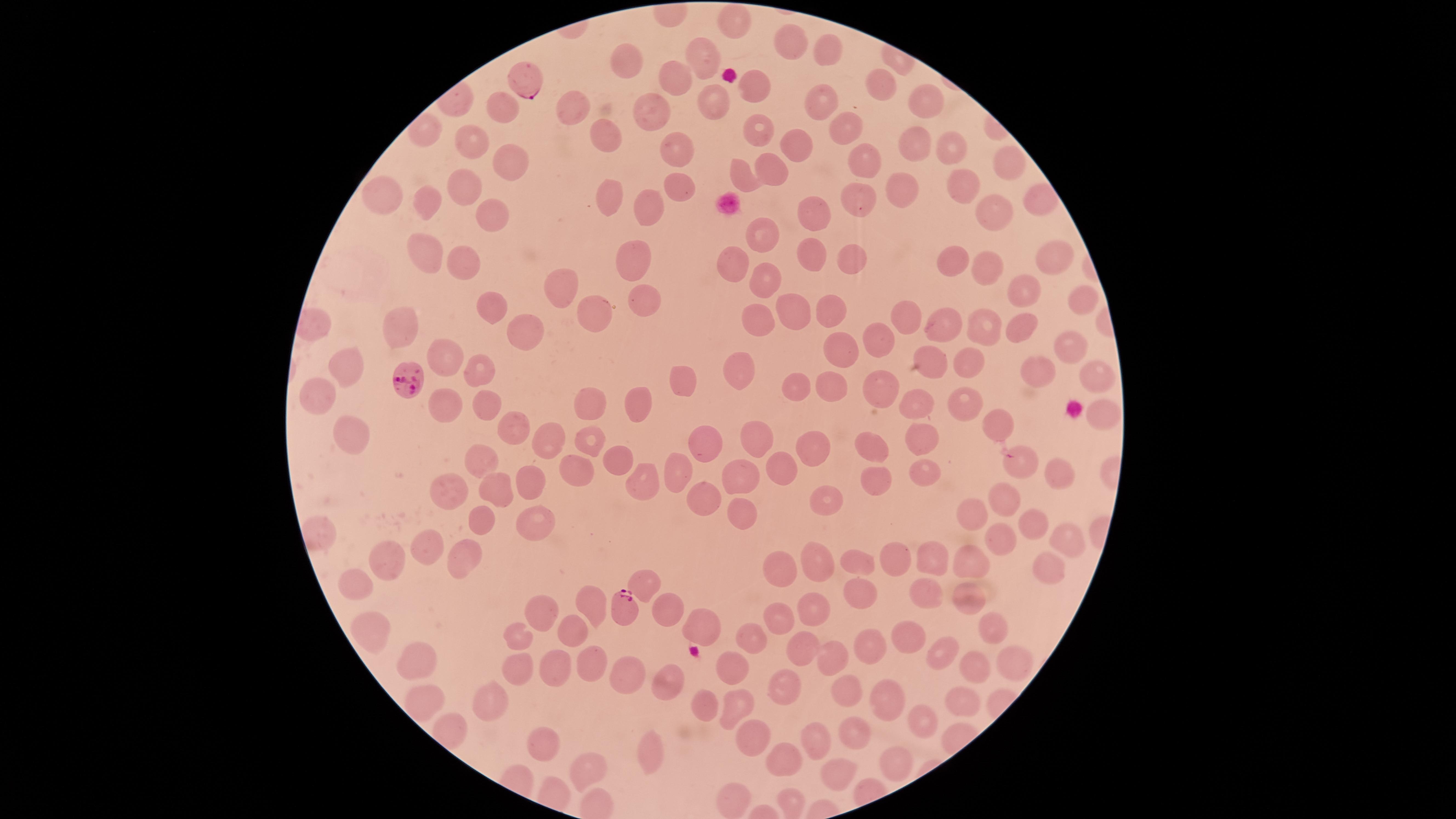

Approximate marker points as (x, y) in pixels.
Summary:
  - Parasitized red blood cells: (526, 73), (409, 384), (625, 611)
  - Uninfected red blood cells: (733, 25), (792, 40), (829, 50), (699, 61), (624, 66), (675, 78), (881, 84), (753, 89), (829, 100), (714, 104), (923, 105), (503, 110), (571, 113), (649, 115), (759, 130), (846, 130), (611, 138), (916, 145), (472, 146), (677, 146), (798, 148), (951, 148), (864, 153), (503, 167), (1010, 168), (773, 174), (742, 177), (673, 184), (958, 188), (611, 192), (899, 197), (375, 199), (857, 200), (464, 201), (428, 205), (645, 212), (993, 214), (817, 215), (488, 216), (767, 234), (417, 246), (1049, 253), (817, 255), (858, 256), (462, 257), (635, 257), (955, 261), (734, 263), (983, 267), (768, 277), (565, 291), (1020, 295), (649, 300), (1083, 305), (594, 306), (494, 307), (836, 307), (792, 312), (906, 313), (760, 321), (936, 324), (397, 325), (1023, 328), (987, 329), (527, 332), (870, 336), (1067, 345), (843, 353), (445, 357), (930, 357), (971, 361), (346, 362), (483, 365), (743, 368), (1034, 369), (1097, 378), (684, 379), (883, 386), (834, 387), (798, 388), (321, 395), (917, 401), (966, 403), (638, 404), (590, 405), (488, 409), (1098, 412), (444, 415), (997, 426), (517, 429), (351, 431), (924, 437), (585, 439), (755, 440), (545, 441), (702, 444), (811, 445), (871, 449), (616, 459), (484, 461), (778, 464), (1023, 467), (681, 468), (920, 473), (1058, 473), (743, 476), (530, 479), (571, 481), (640, 485), (874, 487), (501, 489), (454, 491), (825, 492), (702, 496), (1007, 500), (743, 504), (974, 513), (534, 516), (1029, 519), (483, 520), (1062, 537), (1001, 543), (422, 550), (468, 554), (385, 557), (895, 561), (822, 562), (928, 562), (968, 562), (861, 564), (1048, 564), (784, 568), (643, 582), (360, 583), (920, 591), (860, 594), (969, 599), (586, 600), (815, 603), (665, 606), (538, 607), (782, 616), (697, 621), (577, 626), (990, 626), (373, 627), (515, 635), (752, 638), (909, 640), (863, 650), (944, 651), (801, 654), (423, 655), (829, 657), (1017, 660), (594, 664), (972, 666), (559, 668), (733, 668), (520, 670), (624, 673), (670, 679), (786, 689), (843, 692), (424, 699), (495, 701), (882, 702), (964, 702), (704, 703), (735, 706), (924, 721), (856, 729), (753, 741), (812, 741), (544, 745), (650, 751), (788, 760), (895, 761), (586, 770), (837, 773), (736, 793)
  - Preparation: thin blood smear
  - Image size: 1456×819 pixels
  - Presence: malaria parasites detected
  - Stain: Giemsa
  - Visible region: circular
  - Capture: smartphone photograph through the microscope eyepiece
  - Species: Plasmodium falciparum
  - Field of view: single